Report the malaria status of this cell.
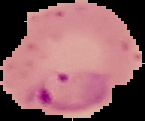
It is parasitized.

Segmented cell region on a black background. Image is 145×121 pixels. From a thin blood film.